State the blood parasite species.
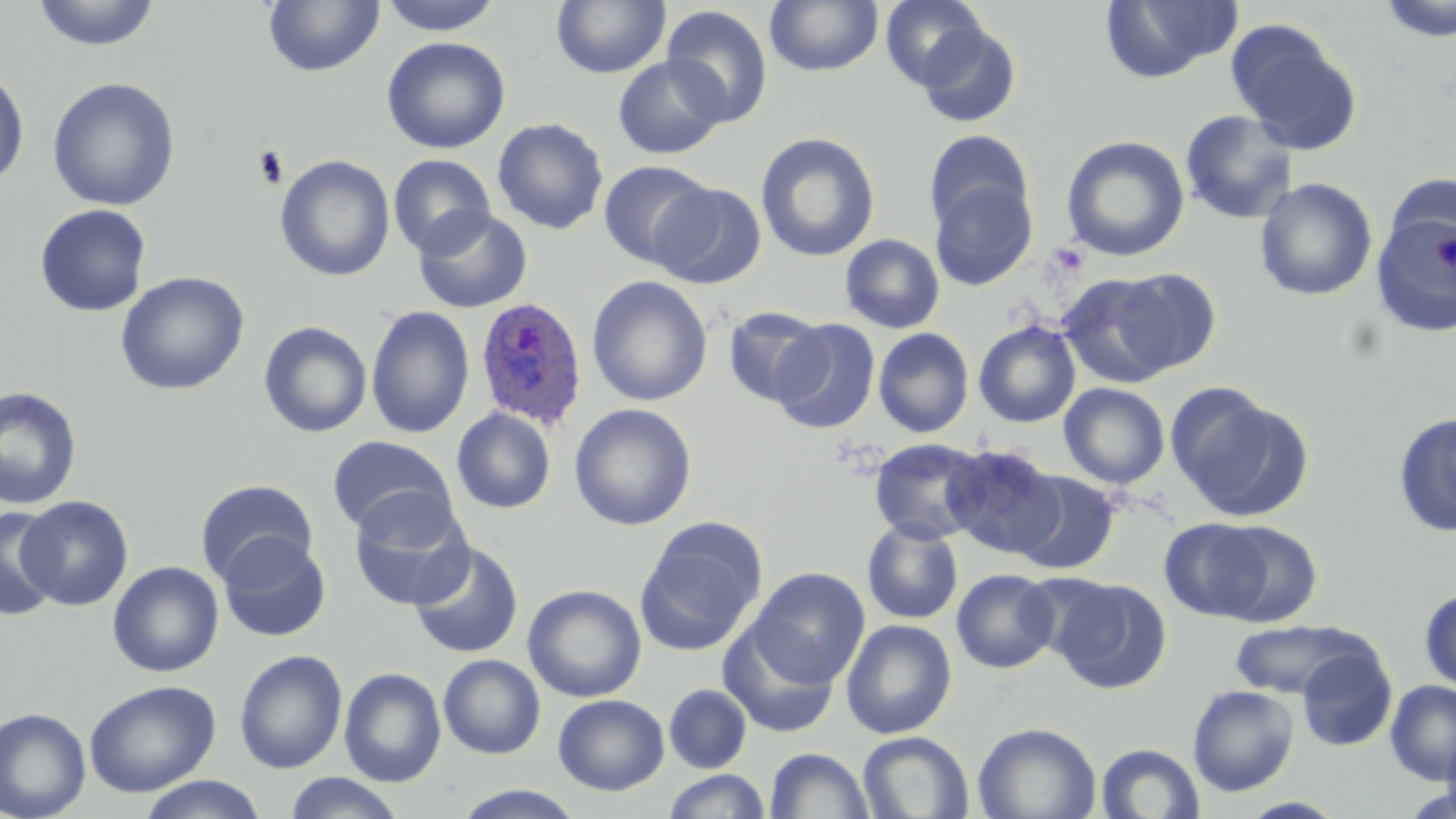
Plasmodium ovale.

Summary:
  - Coordinate format: approximate bounding boxes as named x1/y1/x2/y2 corners in pixels
  - Uninfected red blood cell locations: (x1=31, y1=0, x2=162, y2=51), (x1=263, y1=0, x2=385, y2=77), (x1=378, y1=0, x2=504, y2=35), (x1=880, y1=0, x2=989, y2=91), (x1=1377, y1=0, x2=1456, y2=42), (x1=551, y1=1, x2=670, y2=78), (x1=764, y1=1, x2=884, y2=76), (x1=1100, y1=1, x2=1242, y2=82), (x1=660, y1=5, x2=774, y2=127), (x1=1226, y1=21, x2=1362, y2=154), (x1=916, y1=22, x2=1022, y2=128), (x1=381, y1=36, x2=510, y2=154), (x1=613, y1=56, x2=727, y2=159), (x1=0, y1=66, x2=30, y2=187), (x1=47, y1=76, x2=181, y2=211), (x1=1179, y1=109, x2=1299, y2=225), (x1=492, y1=117, x2=609, y2=234), (x1=924, y1=130, x2=1034, y2=239), (x1=755, y1=132, x2=880, y2=262), (x1=1061, y1=135, x2=1190, y2=262), (x1=387, y1=154, x2=495, y2=258), (x1=275, y1=155, x2=395, y2=282), (x1=598, y1=160, x2=717, y2=269), (x1=928, y1=174, x2=1038, y2=291), (x1=1254, y1=177, x2=1378, y2=300), (x1=651, y1=182, x2=768, y2=289), (x1=1369, y1=202, x2=1456, y2=339), (x1=34, y1=203, x2=152, y2=317), (x1=413, y1=206, x2=533, y2=313), (x1=840, y1=234, x2=945, y2=333), (x1=1104, y1=267, x2=1222, y2=376), (x1=115, y1=270, x2=250, y2=396), (x1=1058, y1=272, x2=1187, y2=388), (x1=586, y1=275, x2=713, y2=407), (x1=366, y1=305, x2=475, y2=439), (x1=722, y1=306, x2=830, y2=408), (x1=771, y1=318, x2=881, y2=434), (x1=974, y1=320, x2=1081, y2=428), (x1=258, y1=321, x2=373, y2=438), (x1=873, y1=327, x2=975, y2=438), (x1=1059, y1=383, x2=1170, y2=489), (x1=0, y1=386, x2=82, y2=510), (x1=1168, y1=388, x2=1314, y2=522), (x1=569, y1=403, x2=697, y2=530), (x1=451, y1=407, x2=556, y2=514), (x1=1393, y1=412, x2=1456, y2=539), (x1=328, y1=435, x2=457, y2=540), (x1=868, y1=437, x2=989, y2=545), (x1=943, y1=444, x2=1064, y2=559), (x1=1010, y1=469, x2=1121, y2=575), (x1=196, y1=479, x2=318, y2=587), (x1=349, y1=495, x2=473, y2=610), (x1=17, y1=496, x2=133, y2=610), (x1=0, y1=505, x2=63, y2=621), (x1=1159, y1=517, x2=1275, y2=622), (x1=635, y1=519, x2=765, y2=655), (x1=862, y1=519, x2=963, y2=624), (x1=1206, y1=520, x2=1323, y2=626), (x1=217, y1=534, x2=331, y2=642), (x1=408, y1=541, x2=524, y2=658), (x1=107, y1=561, x2=224, y2=677), (x1=749, y1=567, x2=870, y2=687), (x1=951, y1=568, x2=1059, y2=674), (x1=1047, y1=576, x2=1172, y2=694), (x1=523, y1=584, x2=647, y2=702), (x1=1419, y1=588, x2=1456, y2=694), (x1=841, y1=619, x2=956, y2=739), (x1=1231, y1=619, x2=1375, y2=700), (x1=718, y1=621, x2=841, y2=738), (x1=1296, y1=646, x2=1398, y2=751), (x1=234, y1=649, x2=347, y2=773), (x1=438, y1=654, x2=545, y2=758), (x1=339, y1=667, x2=446, y2=786), (x1=84, y1=679, x2=220, y2=797), (x1=1385, y1=680, x2=1456, y2=784), (x1=664, y1=683, x2=752, y2=773), (x1=1187, y1=684, x2=1300, y2=797), (x1=554, y1=694, x2=669, y2=795), (x1=0, y1=708, x2=91, y2=819), (x1=972, y1=722, x2=1101, y2=819), (x1=1441, y1=722, x2=1456, y2=819), (x1=857, y1=731, x2=974, y2=818), (x1=1095, y1=742, x2=1206, y2=819), (x1=765, y1=748, x2=874, y2=819), (x1=663, y1=770, x2=771, y2=819), (x1=283, y1=773, x2=406, y2=819), (x1=136, y1=776, x2=268, y2=818), (x1=454, y1=785, x2=587, y2=819)
  - Plasmodium ovale-infected red blood cell locations: (x1=474, y1=297, x2=588, y2=431)
  - Platelet locations: (x1=252, y1=145, x2=288, y2=188)
  - Stain: May-Grünwald-Giemsa
  - Field of view: single
  - Preparation: thin blood film
  - Image size: 1456×819 pixels
  - Magnification: 1000x
  - Modality: light microscopy